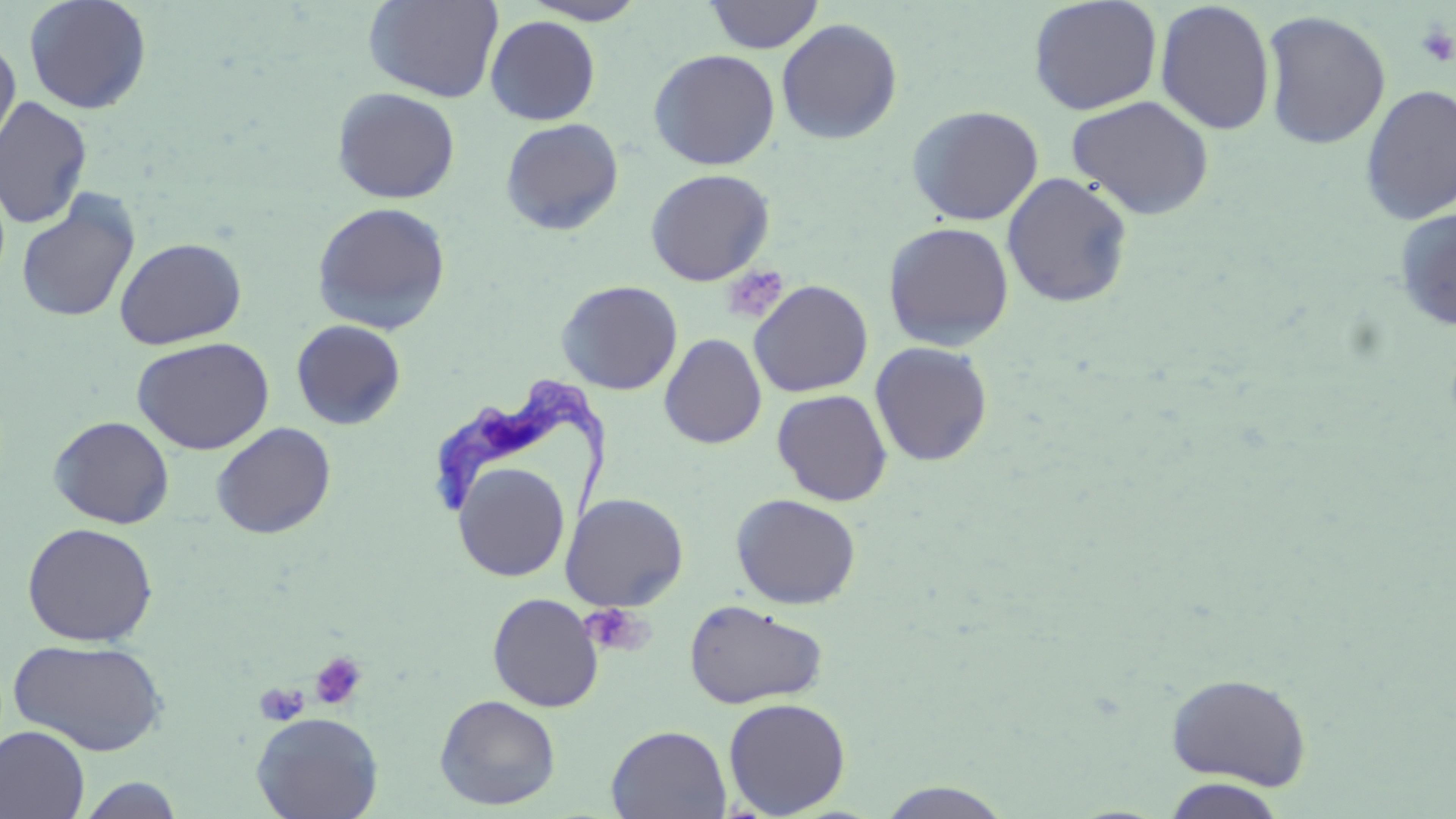

Approximate bounding boxes as named x1/y1/x2/y2 corners in pixels. Uninfected red blood cell locations: (x1=24, y1=0, x2=152, y2=114), (x1=363, y1=0, x2=504, y2=102), (x1=521, y1=0, x2=649, y2=25), (x1=704, y1=0, x2=825, y2=54), (x1=1028, y1=0, x2=1163, y2=115), (x1=1154, y1=1, x2=1276, y2=135), (x1=1260, y1=10, x2=1391, y2=149), (x1=485, y1=16, x2=601, y2=125), (x1=776, y1=18, x2=902, y2=145), (x1=0, y1=41, x2=20, y2=157), (x1=648, y1=49, x2=780, y2=171), (x1=1359, y1=84, x2=1456, y2=225), (x1=332, y1=87, x2=460, y2=204), (x1=1067, y1=95, x2=1214, y2=220), (x1=0, y1=96, x2=92, y2=229), (x1=907, y1=104, x2=1044, y2=226), (x1=900, y1=105, x2=1032, y2=349), (x1=500, y1=117, x2=625, y2=236), (x1=645, y1=168, x2=775, y2=286), (x1=1002, y1=172, x2=1134, y2=308), (x1=15, y1=191, x2=141, y2=324), (x1=311, y1=202, x2=451, y2=335), (x1=1393, y1=208, x2=1456, y2=332), (x1=883, y1=221, x2=1015, y2=351), (x1=114, y1=237, x2=247, y2=349), (x1=556, y1=280, x2=682, y2=395), (x1=749, y1=280, x2=873, y2=397), (x1=291, y1=319, x2=406, y2=430), (x1=660, y1=333, x2=767, y2=449), (x1=132, y1=337, x2=274, y2=455), (x1=869, y1=342, x2=993, y2=466), (x1=772, y1=389, x2=893, y2=506), (x1=48, y1=415, x2=175, y2=528), (x1=210, y1=422, x2=336, y2=539), (x1=453, y1=463, x2=570, y2=582), (x1=560, y1=493, x2=689, y2=611), (x1=731, y1=493, x2=861, y2=609), (x1=22, y1=522, x2=158, y2=646), (x1=487, y1=592, x2=604, y2=712), (x1=683, y1=599, x2=829, y2=709), (x1=8, y1=638, x2=168, y2=756), (x1=1164, y1=672, x2=1313, y2=790), (x1=434, y1=694, x2=561, y2=811), (x1=723, y1=697, x2=851, y2=817), (x1=251, y1=712, x2=383, y2=819), (x1=606, y1=724, x2=732, y2=818), (x1=0, y1=726, x2=90, y2=819), (x1=75, y1=775, x2=187, y2=818), (x1=1161, y1=777, x2=1289, y2=818), (x1=874, y1=781, x2=1017, y2=818). Trypanosoma brucei locations: (x1=427, y1=381, x2=608, y2=526). Platelet locations: (x1=1415, y1=23, x2=1456, y2=68), (x1=720, y1=264, x2=789, y2=324), (x1=581, y1=602, x2=651, y2=656), (x1=308, y1=651, x2=367, y2=711), (x1=255, y1=682, x2=310, y2=725). Slide-level diagnosis: Trypanosoma brucei. Thin blood film. Single field of view. Captured at 1000x magnification. Light microscopy. Image is 1456×819 pixels. May-Grünwald-Giemsa-stained preparation.